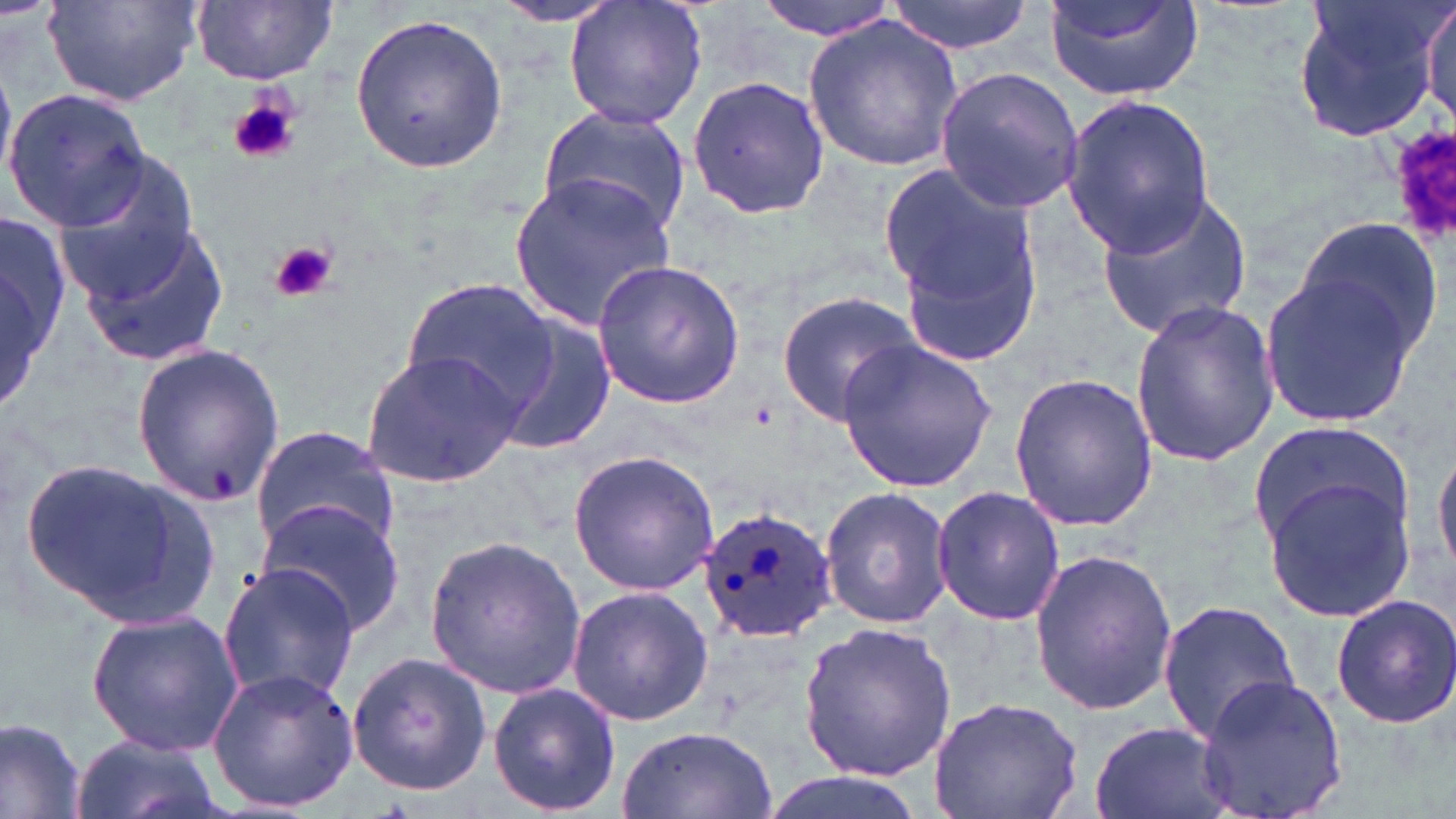

{
  "plasmodium_ovale_infected_red_blood_cell_locations": "approximate bounding boxes as (x1,y1)-(x2,y2) corner pairs in pixels: (698,506)-(837,647)",
  "slide_level_diagnosis": "Plasmodium ovale",
  "uninfected_red_blood_cell_locations": "approximate bounding boxes as (x1,y1)-(x2,y2) corner pairs in pixels: (43,0)-(203,108), (753,0)-(900,40), (883,0)-(1035,55), (1043,0)-(1205,101), (1290,0)-(1451,145), (1421,0)-(1456,129), (192,1)-(338,86), (496,1)-(625,30), (561,1)-(709,131), (347,14)-(509,174), (803,15)-(963,172), (935,67)-(1083,214), (684,74)-(830,222), (5,89)-(154,232), (1062,95)-(1214,255), (537,105)-(693,239), (55,150)-(203,304), (878,159)-(1046,363), (506,169)-(678,331), (1090,187)-(1255,339), (0,205)-(66,425), (1290,211)-(1442,364), (75,220)-(232,368), (590,258)-(747,409), (1256,268)-(1425,427), (402,279)-(560,421), (774,292)-(922,426), (1129,300)-(1280,467), (498,315)-(619,459), (836,337)-(997,493), (130,344)-(286,509), (362,348)-(524,490), (1007,372)-(1158,532), (249,424)-(401,557), (1247,426)-(1413,556), (1434,441)-(1456,583), (567,448)-(720,597), (16,457)-(222,628), (1259,468)-(1418,626), (931,485)-(1065,626), (819,487)-(955,629), (258,499)-(407,634), (423,531)-(587,701), (1026,545)-(1177,716), (217,562)-(362,707), (564,585)-(714,727), (1329,594)-(1456,730), (1156,598)-(1302,748), (85,610)-(244,757), (798,620)-(958,780), (346,651)-(492,798), (207,668)-(360,813), (1194,672)-(1349,819), (488,682)-(622,814), (927,694)-(1088,819), (0,716)-(88,819), (1089,722)-(1236,819), (616,726)-(777,819), (68,735)-(229,819), (757,772)-(935,819)",
  "platelet_locations": "approximate bounding boxes as (x1,y1)-(x2,y2) corner pairs in pixels: (228,94)-(301,166), (1386,123)-(1456,251), (269,242)-(336,303)",
  "field_of_view": "single",
  "preparation": "thin blood film",
  "modality": "optical microscopy",
  "stain": "May-Grünwald-Giemsa",
  "image_size": "1456×819 pixels",
  "magnification": "1000x"
}